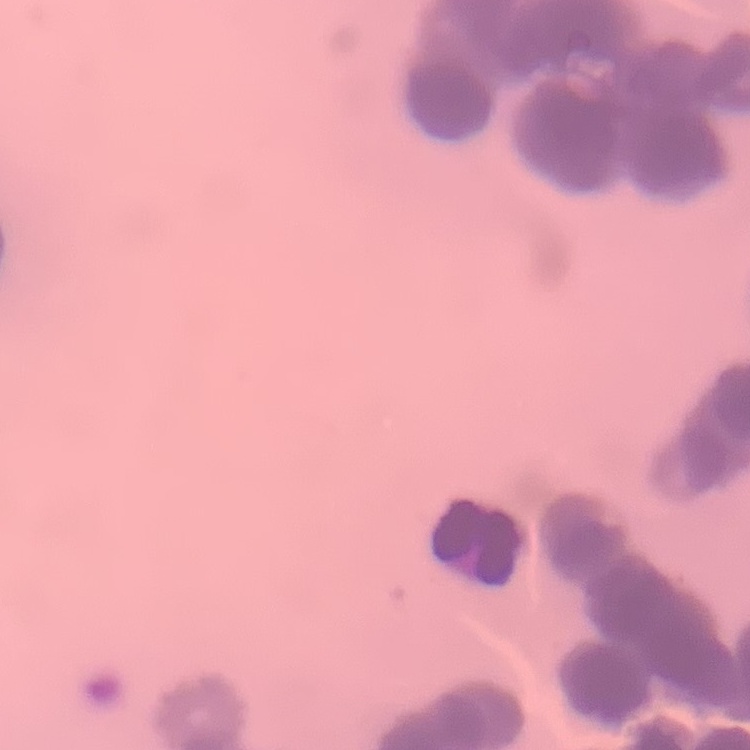 The red blood cells exhibit rouleaux formation. Square crop of a larger photomicrograph. Thin peripheral smear. Stained with either Field's or Giemsa.